Describe the morphology of the red blood cells.
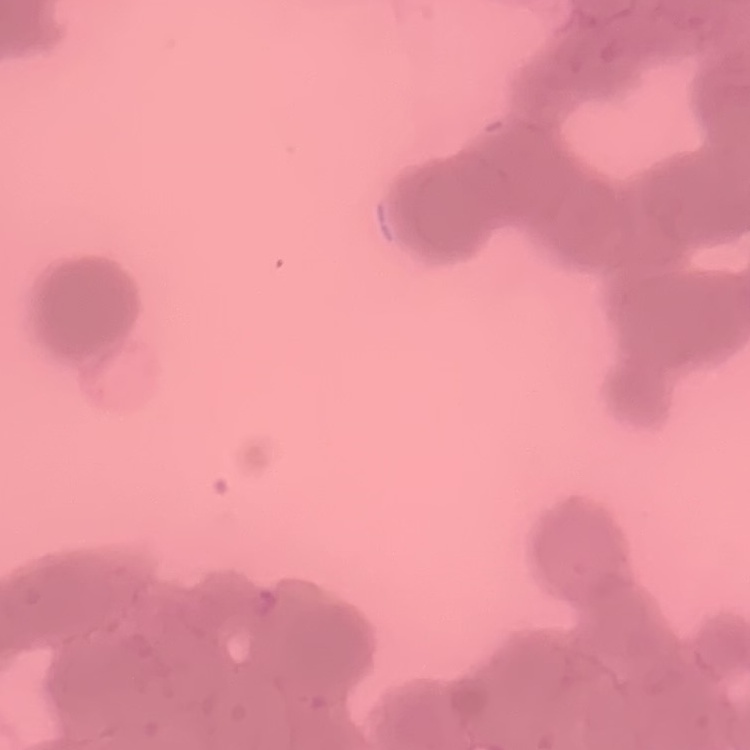
They show rouleaux formation.

{
  "stain": "Field's or Giemsa",
  "preparation": "thin blood film",
  "image_type": "square crop of a larger photomicrograph"
}